Locate every Plasmodium vivax-infected red blood cell.
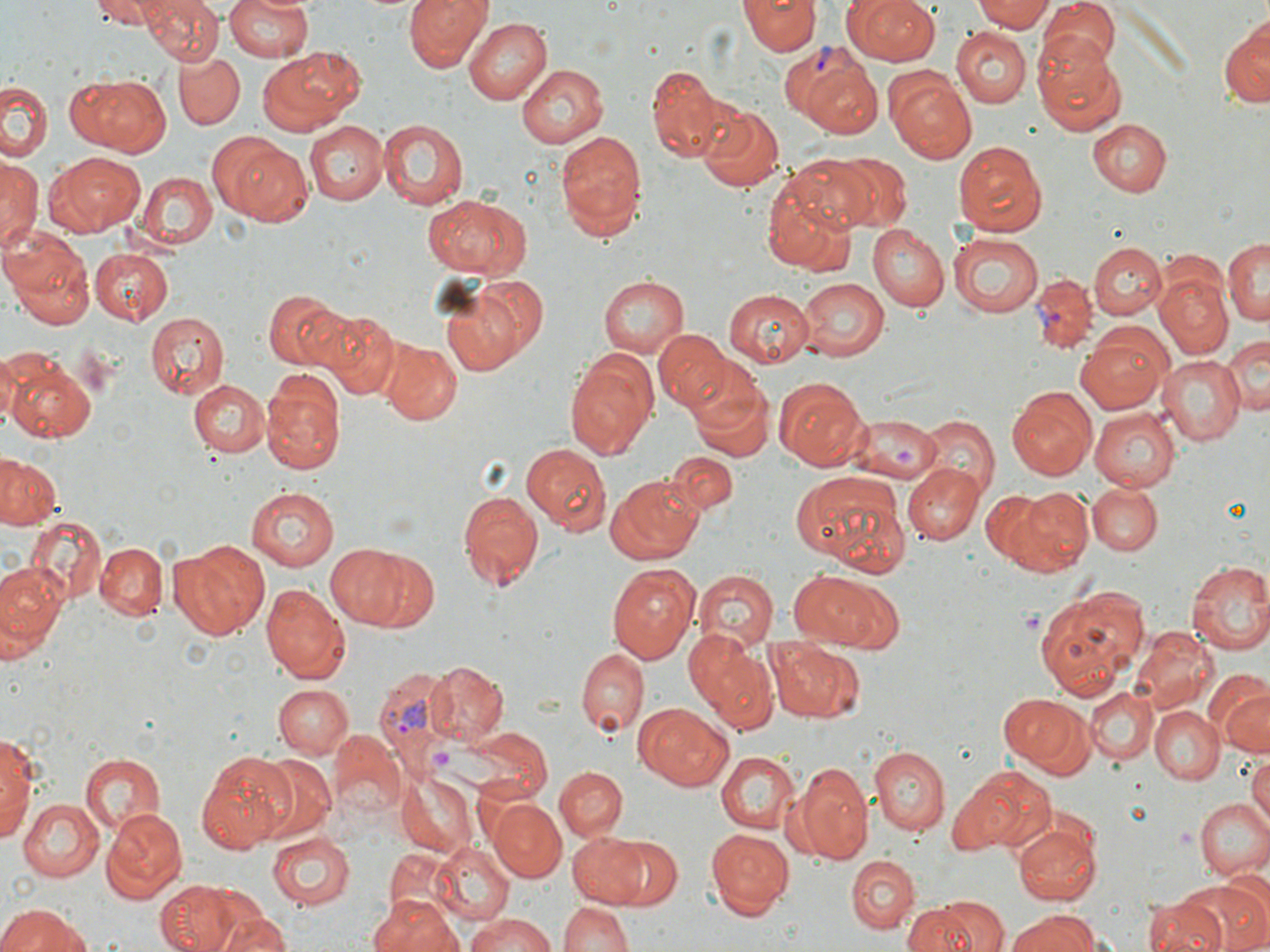
Approximate bounding boxes as (x1, y1, x2, y2) in pixels.
Plasmodium vivax-infected red blood cells: (783, 44, 873, 118), (1030, 275, 1096, 352), (375, 667, 457, 773).

slide_level_diagnosis: Plasmodium vivax
stain: May-Grünwald-Giemsa
image_size: 1270×952 pixels
platelet_locations: 'approximate bounding boxes as (x1, y1, x2, y2) in pixels: (1017, 608, 1044, 635)'
magnification: 1000x
preparation: thin blood film
uninfected_red_blood_cell_locations: 'approximate bounding boxes as (x1, y1, x2, y2) in pixels: (91, 0, 166, 28), (144, 0, 224, 65), (224, 0, 315, 63), (406, 0, 491, 73), (841, 0, 944, 65), (971, 0, 1053, 33), (740, 1, 818, 55), (1038, 1, 1121, 72), (1223, 16, 1270, 110), (463, 17, 554, 105), (951, 27, 1031, 107), (1033, 32, 1123, 133), (256, 48, 366, 136), (175, 51, 244, 129), (644, 62, 734, 160), (515, 63, 608, 149), (805, 65, 882, 137), (885, 75, 977, 163), (65, 76, 171, 156), (0, 83, 49, 164), (697, 104, 784, 193), (377, 118, 466, 209), (304, 119, 388, 205), (1088, 119, 1171, 197), (555, 132, 648, 234), (954, 141, 1047, 235), (229, 143, 311, 227), (45, 151, 146, 237), (835, 154, 911, 230), (1, 155, 41, 255), (786, 157, 887, 234), (136, 171, 217, 250), (760, 179, 858, 276), (422, 193, 527, 278), (869, 226, 949, 311), (2, 227, 95, 327), (948, 234, 1042, 316), (1225, 237, 1270, 330), (1089, 242, 1166, 319), (90, 248, 173, 323), (597, 274, 689, 357), (1156, 274, 1234, 357), (798, 278, 889, 361), (437, 284, 531, 377), (263, 287, 349, 369), (723, 289, 815, 366), (318, 306, 401, 399), (146, 311, 227, 399), (654, 330, 731, 414), (1074, 330, 1172, 414), (1223, 334, 1270, 416), (381, 342, 460, 424), (0, 351, 20, 430), (565, 353, 657, 462), (1155, 355, 1245, 445), (5, 357, 98, 442), (261, 368, 346, 474), (685, 368, 772, 460), (774, 377, 867, 471), (187, 378, 270, 457), (1008, 386, 1096, 480), (1090, 410, 1179, 491), (915, 415, 999, 493), (522, 443, 611, 535), (0, 453, 63, 530), (667, 453, 735, 514), (902, 462, 984, 544), (791, 468, 911, 576), (606, 477, 702, 564), (1086, 483, 1161, 554), (456, 486, 542, 588), (1012, 486, 1095, 572), (245, 487, 338, 569), (979, 489, 1055, 567), (25, 515, 107, 603), (167, 541, 269, 641), (97, 542, 167, 622), (326, 543, 416, 629), (360, 551, 442, 636), (1185, 560, 1270, 656), (0, 561, 67, 660), (607, 562, 700, 664), (693, 569, 778, 648), (788, 571, 902, 651), (259, 583, 350, 684), (1034, 583, 1149, 696), (1132, 627, 1218, 713), (685, 632, 781, 734), (766, 640, 864, 723), (576, 648, 647, 737), (423, 660, 510, 746), (272, 683, 353, 759), (1214, 684, 1270, 760), (1086, 686, 1158, 764), (997, 691, 1094, 777), (635, 704, 734, 791), (1151, 706, 1222, 784), (454, 727, 553, 805), (0, 729, 40, 850), (331, 731, 407, 821), (869, 746, 948, 835), (198, 749, 294, 853), (77, 750, 165, 836), (716, 751, 799, 835), (252, 755, 335, 842), (1246, 755, 1270, 831), (789, 760, 874, 864), (559, 765, 641, 900), (555, 766, 627, 839), (951, 766, 1054, 856), (396, 774, 476, 855), (1196, 797, 1270, 879), (20, 798, 103, 881), (489, 799, 567, 881), (102, 807, 187, 901), (1014, 820, 1100, 904), (707, 829, 794, 914), (567, 831, 650, 908), (269, 834, 353, 908), (601, 838, 681, 909), (429, 842, 515, 927), (383, 848, 456, 921), (846, 854, 919, 934), (1183, 874, 1270, 952), (155, 880, 239, 952), (191, 887, 275, 951), (372, 893, 463, 952), (910, 895, 1002, 952), (1146, 896, 1225, 952), (560, 899, 632, 952), (0, 903, 97, 952), (216, 909, 289, 952), (1008, 911, 1100, 952), (464, 914, 563, 952)'
field_of_view: one of a larger specimen
modality: optical microscopy